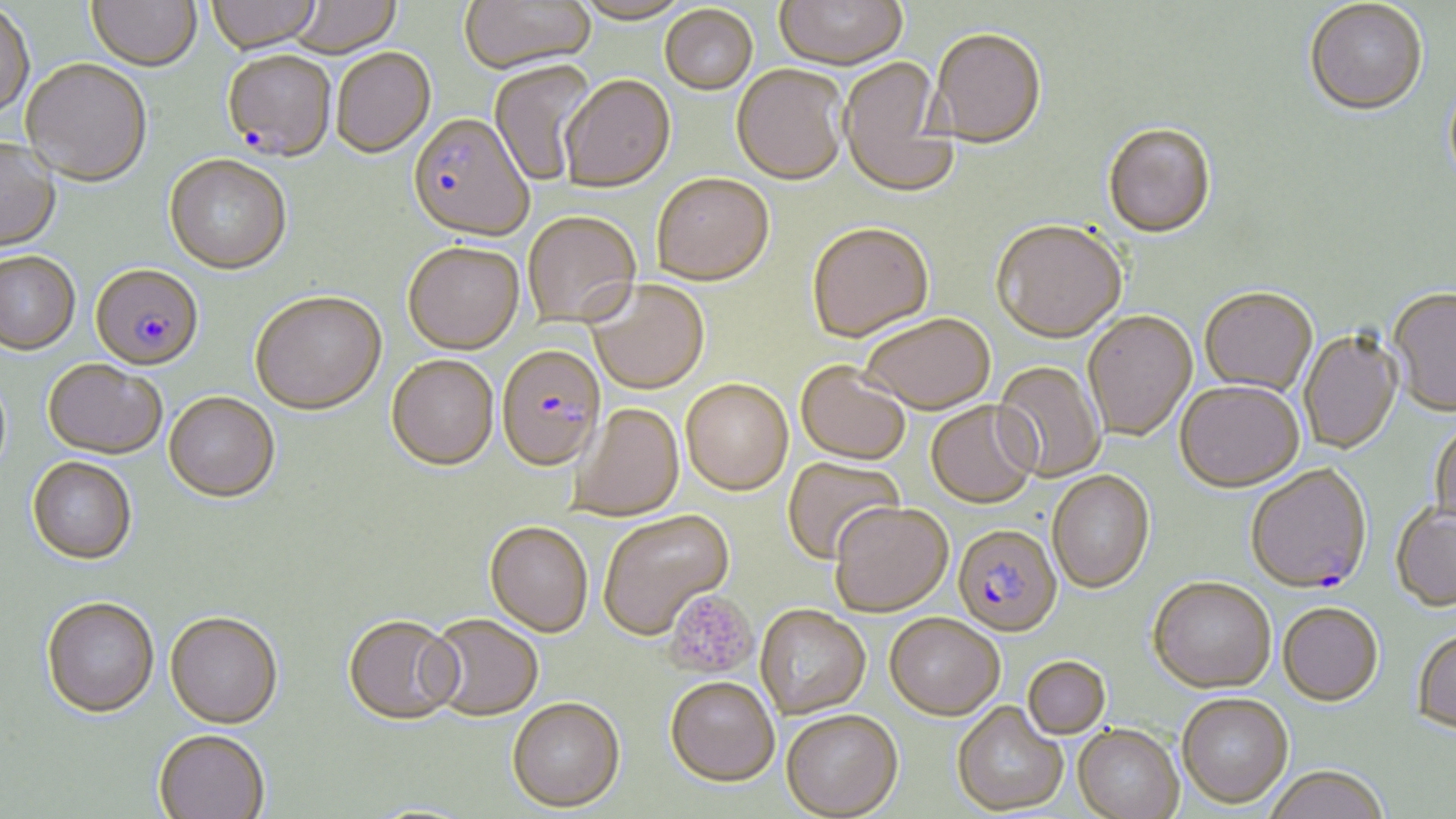
{
  "slide_level_diagnosis": "Plasmodium falciparum",
  "field_of_view": "one of a larger specimen",
  "magnification": "1000x",
  "preparation": "thin blood film",
  "platelet_locations": "approximate bounding boxes as named x1/y1/x2/y2 corners in pixels: (x1=664, y1=590, x2=758, y2=679)",
  "plasmodium_falciparum_infected_red_blood_cell_locations": "approximate bounding boxes as named x1/y1/x2/y2 corners in pixels: (x1=222, y1=54, x2=336, y2=163), (x1=407, y1=115, x2=533, y2=242), (x1=90, y1=264, x2=205, y2=372), (x1=497, y1=345, x2=605, y2=472), (x1=1247, y1=466, x2=1371, y2=595), (x1=955, y1=526, x2=1065, y2=639)",
  "stain": "May-Grünwald-Giemsa",
  "modality": "optical microscopy",
  "uninfected_red_blood_cell_locations": "approximate bounding boxes as named x1/y1/x2/y2 corners in pixels: (x1=86, y1=0, x2=201, y2=74), (x1=207, y1=0, x2=322, y2=56), (x1=284, y1=0, x2=402, y2=58), (x1=459, y1=0, x2=595, y2=76), (x1=775, y1=0, x2=908, y2=73), (x1=570, y1=2, x2=695, y2=27), (x1=1304, y1=2, x2=1428, y2=119), (x1=0, y1=4, x2=35, y2=122), (x1=660, y1=7, x2=758, y2=97), (x1=929, y1=31, x2=1046, y2=150), (x1=331, y1=50, x2=436, y2=160), (x1=839, y1=59, x2=957, y2=198), (x1=21, y1=61, x2=152, y2=189), (x1=488, y1=62, x2=600, y2=187), (x1=731, y1=67, x2=848, y2=187), (x1=560, y1=77, x2=676, y2=194), (x1=1443, y1=78, x2=1456, y2=196), (x1=1103, y1=125, x2=1217, y2=241), (x1=0, y1=140, x2=61, y2=254), (x1=164, y1=156, x2=292, y2=276), (x1=652, y1=175, x2=774, y2=287), (x1=523, y1=213, x2=641, y2=330), (x1=991, y1=222, x2=1126, y2=345), (x1=807, y1=224, x2=934, y2=344), (x1=403, y1=243, x2=524, y2=355), (x1=1, y1=254, x2=80, y2=356), (x1=587, y1=282, x2=710, y2=396), (x1=1200, y1=290, x2=1317, y2=398), (x1=1388, y1=290, x2=1456, y2=419), (x1=250, y1=292, x2=386, y2=416), (x1=1083, y1=312, x2=1197, y2=443), (x1=859, y1=315, x2=995, y2=415), (x1=1299, y1=332, x2=1403, y2=455), (x1=386, y1=356, x2=498, y2=472), (x1=43, y1=361, x2=166, y2=461), (x1=993, y1=361, x2=1105, y2=482), (x1=796, y1=363, x2=911, y2=466), (x1=681, y1=380, x2=794, y2=496), (x1=1174, y1=383, x2=1304, y2=494), (x1=164, y1=393, x2=280, y2=504), (x1=926, y1=402, x2=1039, y2=509), (x1=569, y1=403, x2=685, y2=521), (x1=1428, y1=423, x2=1456, y2=533), (x1=782, y1=456, x2=904, y2=565), (x1=26, y1=458, x2=136, y2=566), (x1=1048, y1=471, x2=1156, y2=595), (x1=830, y1=502, x2=953, y2=617), (x1=1391, y1=507, x2=1456, y2=614), (x1=598, y1=509, x2=734, y2=640), (x1=485, y1=522, x2=593, y2=637), (x1=1148, y1=578, x2=1276, y2=695), (x1=41, y1=598, x2=159, y2=719), (x1=1278, y1=604, x2=1383, y2=708), (x1=755, y1=605, x2=871, y2=719), (x1=164, y1=613, x2=283, y2=729), (x1=884, y1=614, x2=1004, y2=721), (x1=426, y1=615, x2=544, y2=721), (x1=343, y1=616, x2=463, y2=726), (x1=1411, y1=631, x2=1456, y2=739), (x1=1023, y1=656, x2=1111, y2=739), (x1=665, y1=677, x2=779, y2=786), (x1=1177, y1=694, x2=1293, y2=810), (x1=506, y1=698, x2=625, y2=812), (x1=951, y1=703, x2=1067, y2=816), (x1=781, y1=710, x2=903, y2=818), (x1=1072, y1=725, x2=1184, y2=819), (x1=153, y1=729, x2=270, y2=819), (x1=1264, y1=770, x2=1390, y2=819)",
  "image_size": "1456×819 pixels"
}